Point out each Plasmodium parasite.
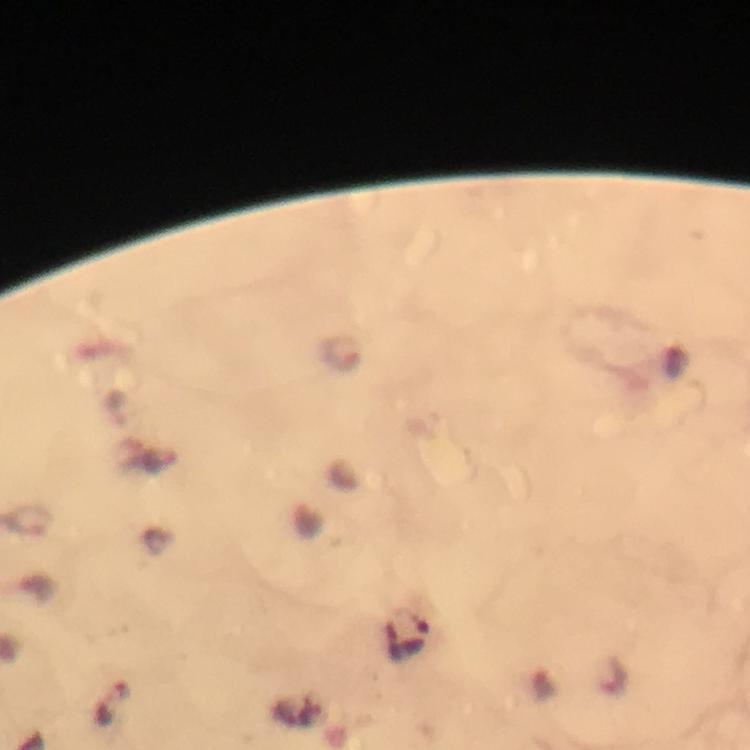
Approximate object centers, in pixels from the top-left corner.
Plasmodium parasites: (x=342, y=353), (x=31, y=520), (x=615, y=676).

Smartphone photograph taken through a microscope. Image is 750×750 pixels. A crop from one field of view. Immersion oil was used. Thick blood film. From a diagnostic examination for malaria. 100x magnification. Giemsa-stained preparation.